Classify this cell by malaria status.
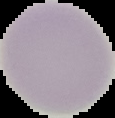

It is uninfected.

Image is 115×118 pixels. The area outside the segmented cell region is set to black. From a thin blood film.